Give the position of every malaria parasite.
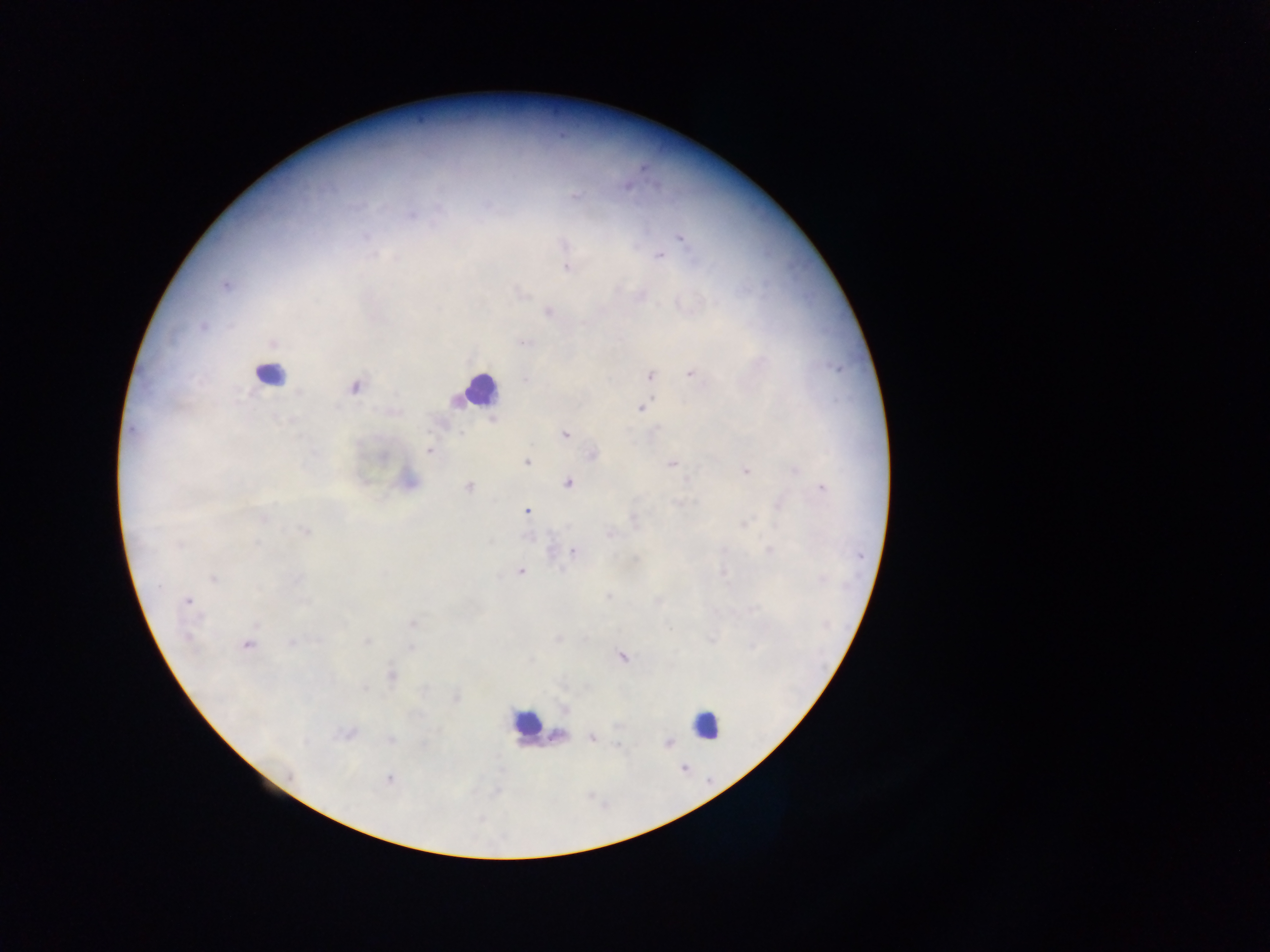

Approximate centers as (x, y) in pixels.
Malaria parasites: (573, 196), (411, 215), (365, 236), (681, 238), (564, 246), (374, 255), (660, 256), (568, 269), (225, 285), (548, 311), (203, 325), (272, 342), (524, 342), (650, 375), (692, 375), (526, 379), (353, 387), (642, 408), (133, 430), (565, 434), (429, 451), (593, 454), (527, 462), (671, 463), (795, 470), (744, 471), (686, 480), (568, 483), (468, 487), (822, 488), (678, 503), (780, 506), (527, 511), (263, 517), (632, 519), (744, 524), (305, 531), (610, 533), (178, 546), (770, 551), (574, 552), (636, 559), (521, 572), (724, 573), (213, 578), (296, 579), (822, 580), (158, 586), (608, 596), (187, 601), (304, 602), (658, 602), (413, 624), (257, 625), (188, 637), (558, 638), (712, 640), (316, 641), (366, 642), (291, 643), (248, 645), (753, 647), (411, 648), (622, 656), (393, 675), (364, 688), (456, 698), (565, 708), (345, 734), (558, 735), (591, 738), (390, 739), (668, 743), (618, 746), (290, 776), (389, 779).

field of view = single
leukocyte locations = approximate centers as (x, y) in pixels: (270, 375), (479, 390), (525, 723), (707, 724)
capture = mobile-phone photograph through a microscope
image size = 1270×952 pixels
preparation = thick blood film
country = Ghana